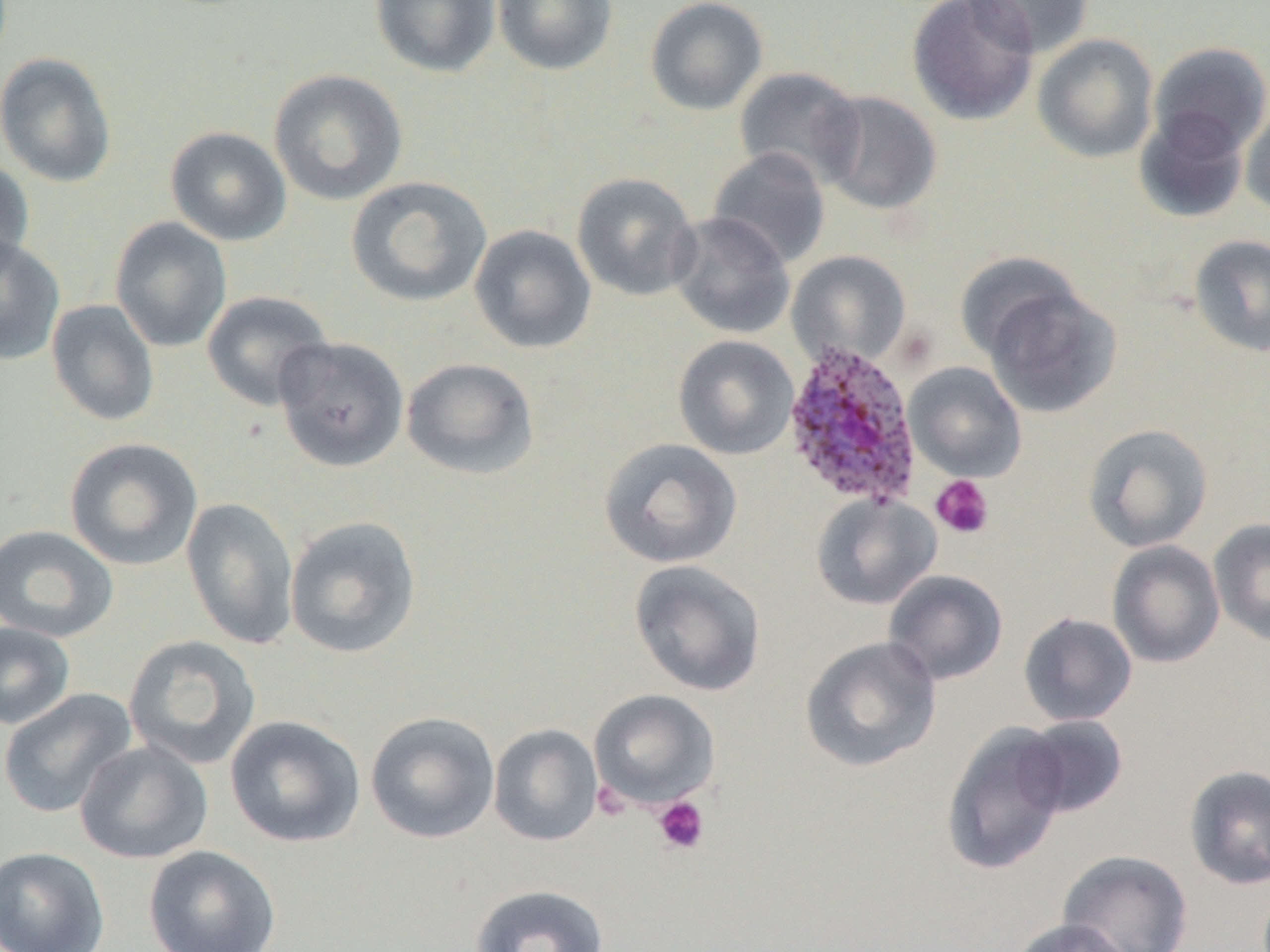
Summary:
  - Coordinate format: approximate bounding boxes as (x1, y1, x2, y2) in pixels
  - Platelet locations: (930, 474, 994, 539), (593, 782, 630, 821), (652, 796, 709, 855)
  - Uninfected red blood cell locations: (370, 0, 501, 78), (492, 0, 618, 75), (645, 0, 769, 116), (906, 0, 1039, 126), (963, 0, 1095, 57), (1033, 34, 1159, 162), (1149, 42, 1270, 158), (0, 52, 118, 188), (734, 66, 865, 188), (268, 69, 408, 206), (816, 90, 943, 216), (1240, 101, 1270, 219), (1134, 108, 1249, 223), (165, 126, 291, 246), (707, 148, 831, 270), (0, 156, 35, 278), (571, 172, 702, 302), (346, 175, 492, 308), (669, 212, 795, 339), (109, 217, 232, 353), (469, 224, 596, 354), (0, 234, 66, 367), (1188, 234, 1270, 357), (787, 250, 911, 370), (954, 251, 1082, 365), (982, 281, 1122, 419), (201, 290, 333, 412), (46, 299, 160, 427), (673, 335, 799, 460), (274, 336, 409, 472), (401, 357, 540, 479), (904, 362, 1026, 482), (1082, 423, 1213, 553), (64, 437, 203, 571), (599, 437, 742, 569), (810, 492, 941, 610), (181, 497, 299, 650), (284, 516, 422, 659), (1209, 517, 1270, 647), (0, 524, 119, 643), (1107, 540, 1225, 668), (629, 559, 766, 697), (884, 569, 1008, 685), (1018, 612, 1138, 726), (0, 621, 76, 730), (123, 635, 262, 770), (800, 635, 942, 773), (0, 687, 138, 818), (589, 689, 721, 810), (365, 711, 500, 844), (224, 714, 365, 848), (1017, 715, 1129, 818), (940, 722, 1071, 875), (488, 723, 603, 846), (74, 740, 214, 864), (1184, 764, 1270, 890), (143, 845, 281, 952), (0, 846, 110, 952), (1058, 849, 1193, 952), (469, 884, 610, 952), (1009, 918, 1137, 952)
  - Plasmodium ovale-infected red blood cell locations: (780, 340, 924, 509)
  - Slide-level diagnosis: Plasmodium ovale
  - Magnification: 1000x
  - Modality: light microscopy
  - Field of view: one of a larger specimen
  - Preparation: thin blood smear
  - Image size: 1270×952 pixels